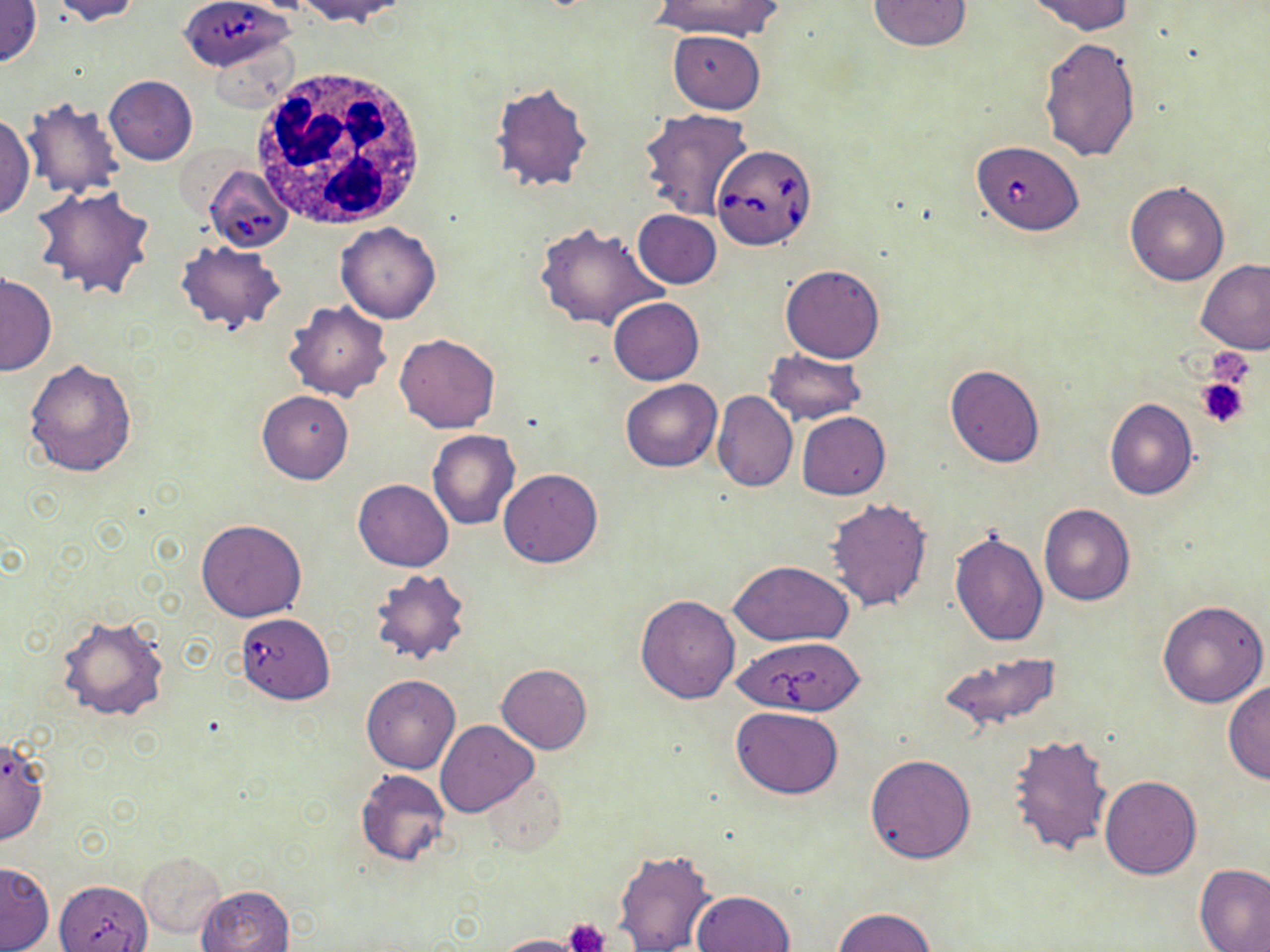 Approximate bounding boxes as [x1, y1, x2, y2] in pixels. Uninfected red blood cell locations: [0, 0, 42, 68], [51, 0, 143, 25], [653, 0, 781, 40], [1029, 0, 1134, 36], [300, 1, 407, 26], [867, 1, 970, 51], [669, 30, 765, 114], [207, 36, 297, 112], [1038, 37, 1141, 162], [104, 76, 197, 165], [491, 82, 594, 192], [20, 98, 125, 199], [638, 108, 755, 221], [0, 111, 34, 222], [1125, 180, 1229, 286], [31, 186, 156, 300], [633, 210, 721, 287], [534, 221, 668, 333], [336, 222, 441, 324], [177, 242, 286, 334], [1196, 261, 1270, 354], [780, 263, 886, 363], [1, 272, 55, 377], [608, 298, 703, 385], [285, 301, 391, 400], [394, 332, 500, 433], [764, 350, 866, 424], [25, 358, 137, 478], [945, 364, 1046, 468], [621, 378, 721, 471], [711, 390, 797, 492], [257, 391, 353, 484], [1104, 398, 1198, 500], [797, 412, 890, 500], [428, 429, 519, 529], [499, 468, 602, 567], [354, 479, 453, 572], [825, 498, 933, 611], [1038, 504, 1135, 606], [195, 519, 306, 621], [949, 528, 1049, 648], [728, 560, 854, 646], [368, 570, 472, 666], [635, 594, 740, 703], [1157, 601, 1268, 707], [57, 615, 169, 720], [941, 652, 1060, 732], [496, 664, 593, 754], [360, 676, 460, 774], [1223, 681, 1270, 783], [731, 706, 844, 799], [434, 719, 536, 816], [1007, 732, 1113, 856], [0, 735, 49, 845], [864, 754, 976, 864], [354, 769, 451, 867], [482, 773, 566, 853], [1100, 776, 1201, 879], [611, 847, 715, 952], [137, 851, 226, 939], [1, 861, 54, 951], [1194, 863, 1270, 952], [197, 885, 293, 952], [692, 889, 795, 952], [835, 908, 936, 951], [555, 921, 615, 951], [490, 934, 588, 952]. Platelet locations: [1204, 347, 1259, 395], [1194, 376, 1250, 428], [566, 917, 610, 952]. Babesia divergens-infected red blood cell locations: [184, 0, 291, 81], [973, 141, 1083, 234], [711, 143, 819, 249], [202, 164, 290, 253], [236, 613, 335, 704], [737, 636, 866, 717], [55, 879, 152, 951]. White blood cell locations: [249, 63, 434, 235]. Slide-level diagnosis: Babesia divergens. Image is 1270×952 pixels. May-Grünwald-Giemsa stain. 1000x magnification. Thin blood smear. One field of a larger specimen. Light microscopy.